Identify the parasite.
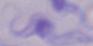
This is a trypanosome.

modality: micrograph
magnification: 1000x